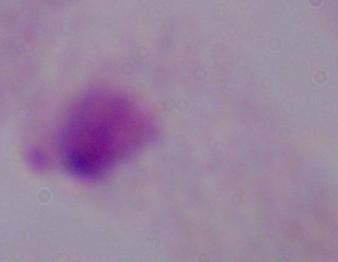
Summary:
  - Modality: photomicrograph
  - Magnification: 1000x
  - Identification: trichomonad